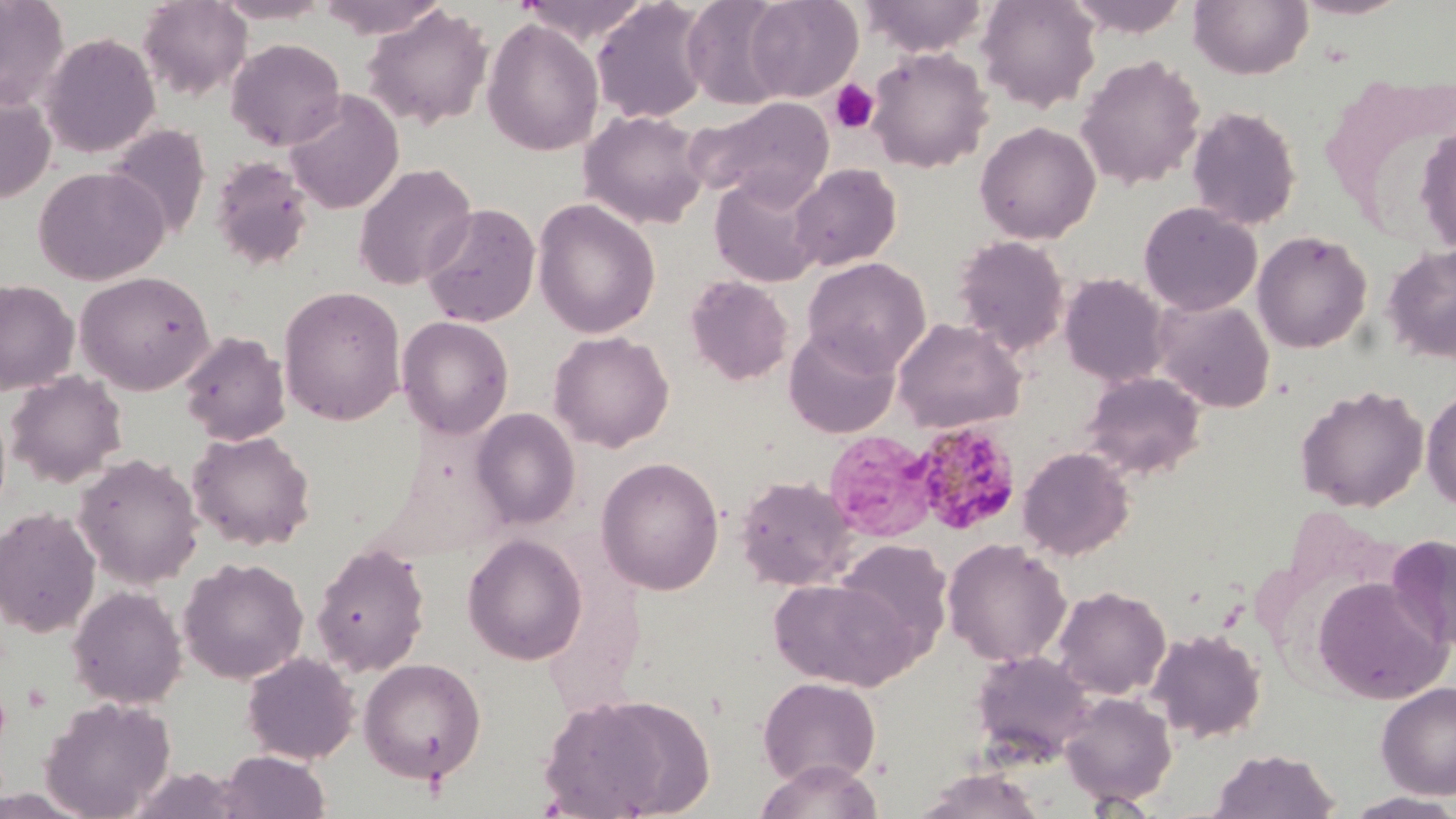
Summary:
  - Coordinate format: approximate bounding boxes as (x1,y1)-(x2,y2) corner pairs in pixels
  - Platelet locations: (827,79)-(880,134)
  - Uninfected red blood cell locations: (0,0)-(70,112), (213,0)-(333,24), (314,0)-(451,39), (516,0)-(654,44), (681,0)-(794,109), (743,0)-(863,102), (861,0)-(989,57), (976,0)-(1101,113), (1064,0)-(1192,37), (1188,0)-(1313,80), (1292,0)-(1411,20), (138,1)-(252,101), (591,1)-(711,124), (362,4)-(494,131), (482,17)-(604,156), (40,32)-(160,158), (226,38)-(346,151), (866,47)-(994,173), (1075,54)-(1206,191), (282,89)-(404,215), (0,91)-(56,204), (686,95)-(835,206), (1187,104)-(1302,231), (579,110)-(709,230), (974,121)-(1101,244), (105,123)-(211,241), (1414,124)-(1456,254), (209,154)-(315,273), (353,162)-(478,291), (789,163)-(902,271), (33,166)-(169,285), (709,172)-(826,288), (532,198)-(661,338), (1138,201)-(1262,316), (420,203)-(541,327), (1252,229)-(1373,353), (952,235)-(1070,355), (1382,244)-(1456,362), (802,257)-(931,375), (74,270)-(215,395), (1059,272)-(1170,387), (685,275)-(793,386), (0,279)-(79,395), (278,286)-(406,426), (1152,297)-(1275,412), (397,315)-(514,439), (892,317)-(1027,433), (784,328)-(900,438), (548,330)-(674,452), (178,331)-(291,446), (5,370)-(128,488), (1081,370)-(1207,480), (1295,385)-(1429,512), (1422,388)-(1456,511), (470,407)-(581,529), (187,429)-(316,551), (824,430)-(938,543), (1017,446)-(1135,561), (73,453)-(204,589), (596,456)-(725,595), (733,475)-(858,591), (0,507)-(101,638), (462,534)-(588,665), (1385,534)-(1456,653), (942,538)-(1072,666), (835,539)-(952,656), (311,540)-(431,677), (179,557)-(309,685), (768,576)-(920,691), (1313,576)-(1450,704), (67,585)-(188,709), (1052,585)-(1171,700), (1146,628)-(1266,743), (970,650)-(1095,764), (241,651)-(360,764), (358,658)-(487,784), (757,675)-(881,788), (1376,681)-(1456,799), (1059,691)-(1178,807), (539,692)-(711,819), (40,696)-(176,817), (1209,748)-(1340,818), (217,750)-(331,819), (753,758)-(884,819), (911,768)-(1048,818), (1341,792)-(1456,818)
  - Plasmodium malariae-infected red blood cell locations: (911,421)-(1022,535)
  - Slide-level diagnosis: Plasmodium malariae
  - Magnification: 1000x
  - Field of view: single
  - Modality: light microscopy
  - Preparation: thin blood smear
  - Stain: May-Grünwald-Giemsa
  - Image size: 1456×819 pixels